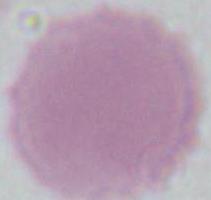

{
  "magnification": "1000x",
  "identification": "red blood cell",
  "modality": "micrograph"
}